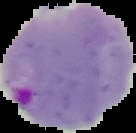
Summary:
  - Image size: 136×133 pixels
  - Image type: segmented cell region on a black background
  - Malaria status: parasitized
  - Preparation: thin blood film